Assess for Plasmodium parasites.
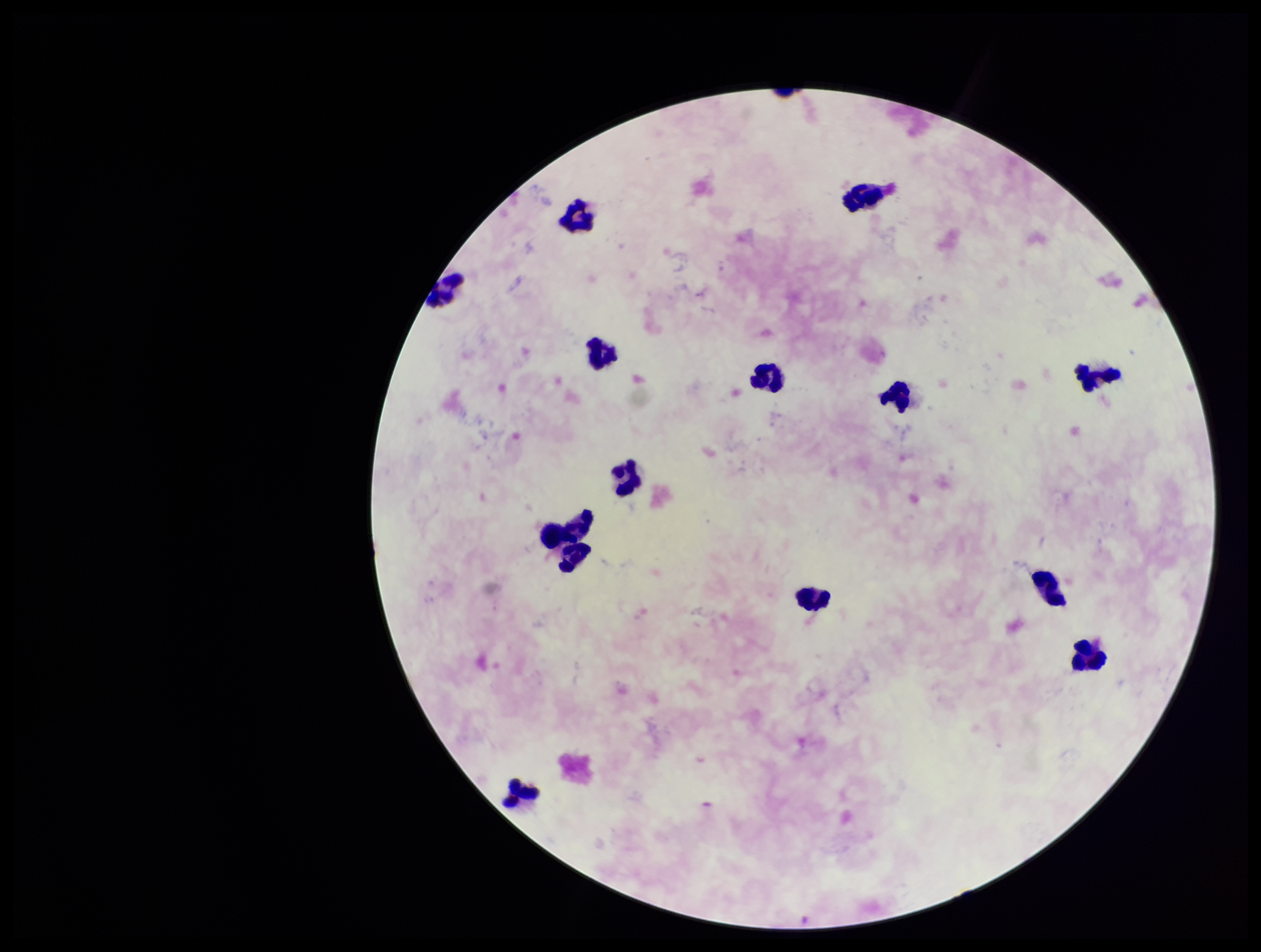
None detected.

preparation = thick smear
image size = 1261×952 pixels
parasite count = 0
leukocyte count = 14
field of view = single
capture = smartphone photograph through the microscope eyepiece
patient malaria status = negative
stain = Giemsa